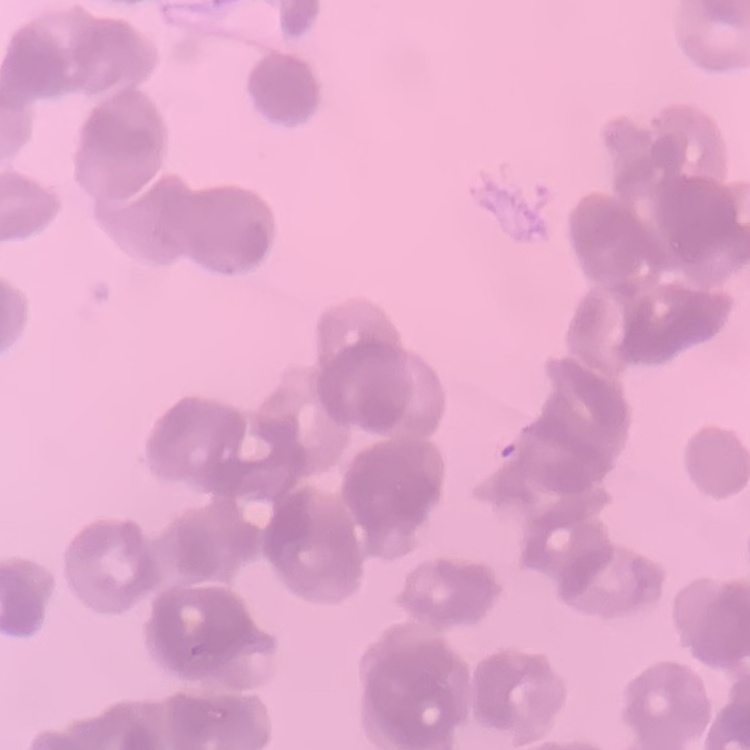
The erythrocytes exhibit rouleaux formation. Thin peripheral smear. Field's or Giemsa stain. One tile cut from a larger photomicrograph.